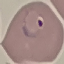

Summary:
  - Malaria status: parasitized
  - Preparation: thin blood smear
  - Capture: smartphone camera at the microscope eyepiece
  - Stain: Giemsa
  - Image type: cell patch, automatically extracted from a larger field of view and resized to 64 × 64 pixels